Assess this cell for malaria.
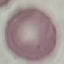
Uninfected.

{
  "capture": "smartphone through the microscope eyepiece",
  "stain": "Giemsa",
  "image_type": "cell patch, automatically extracted from a larger field of view and resized to 64 × 64 pixels",
  "preparation": "thin blood film"
}